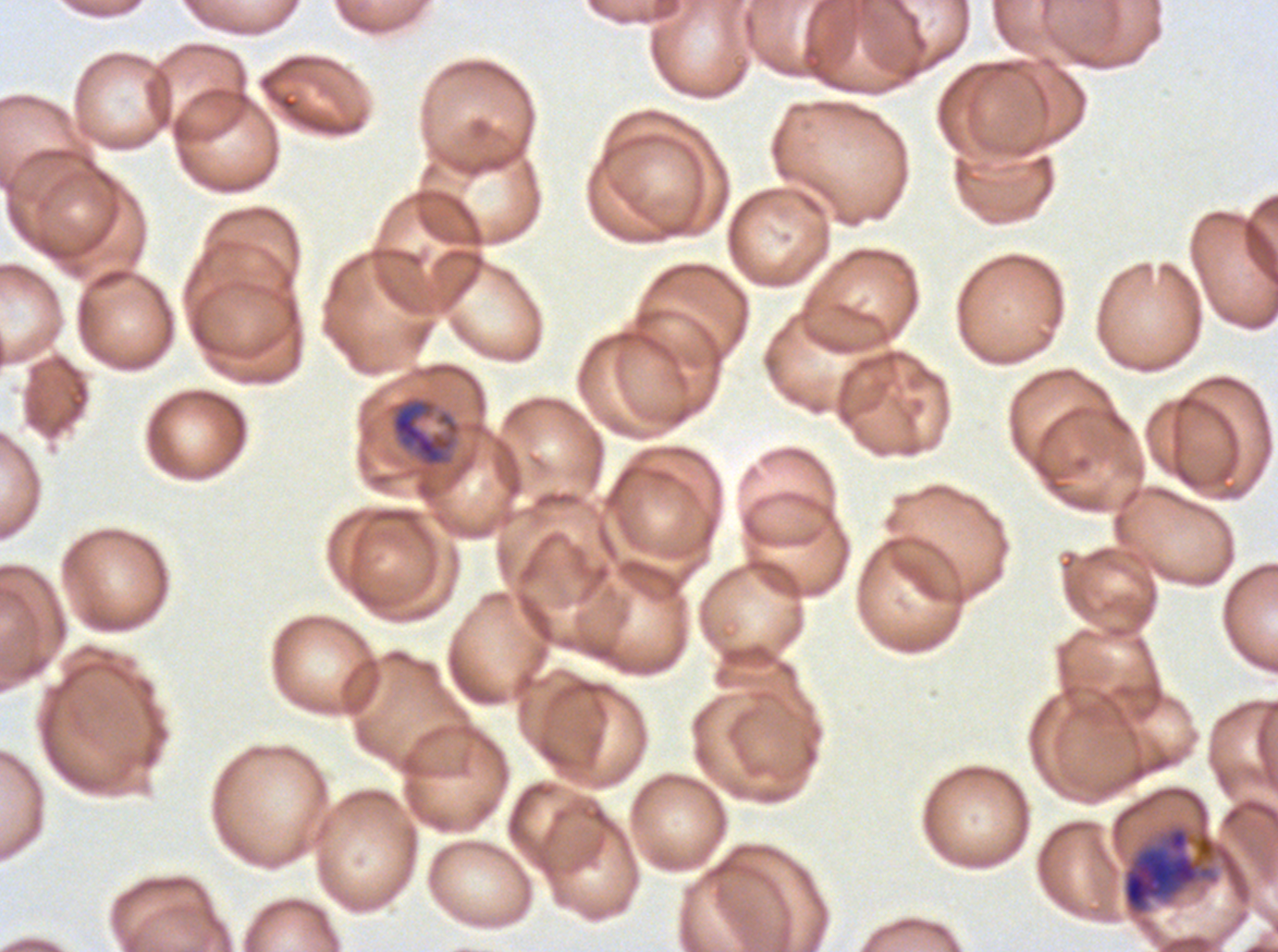 Approximate bounding boxes as [x1, y1, x2, y2] in pixels. Mid trophozoite locations: [390, 397, 455, 467]. Late schizont locations: [1122, 824, 1244, 916]. Image is 1278×952 pixels. Thin blood film. P. falciparum from a patient in The Gambia, cultured ex vivo for 24 to 48 hours. Giemsa-stained preparation. One sub-image of a larger composite. Life-cycle stages observed: mid trophozoite, late schizont.